Identify the cell.
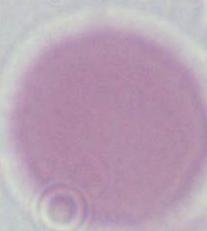
This is an erythrocyte.

Photomicrograph. 1000x magnification.